Locate every malaria parasite by life-cycle stage, and every leukocyte.
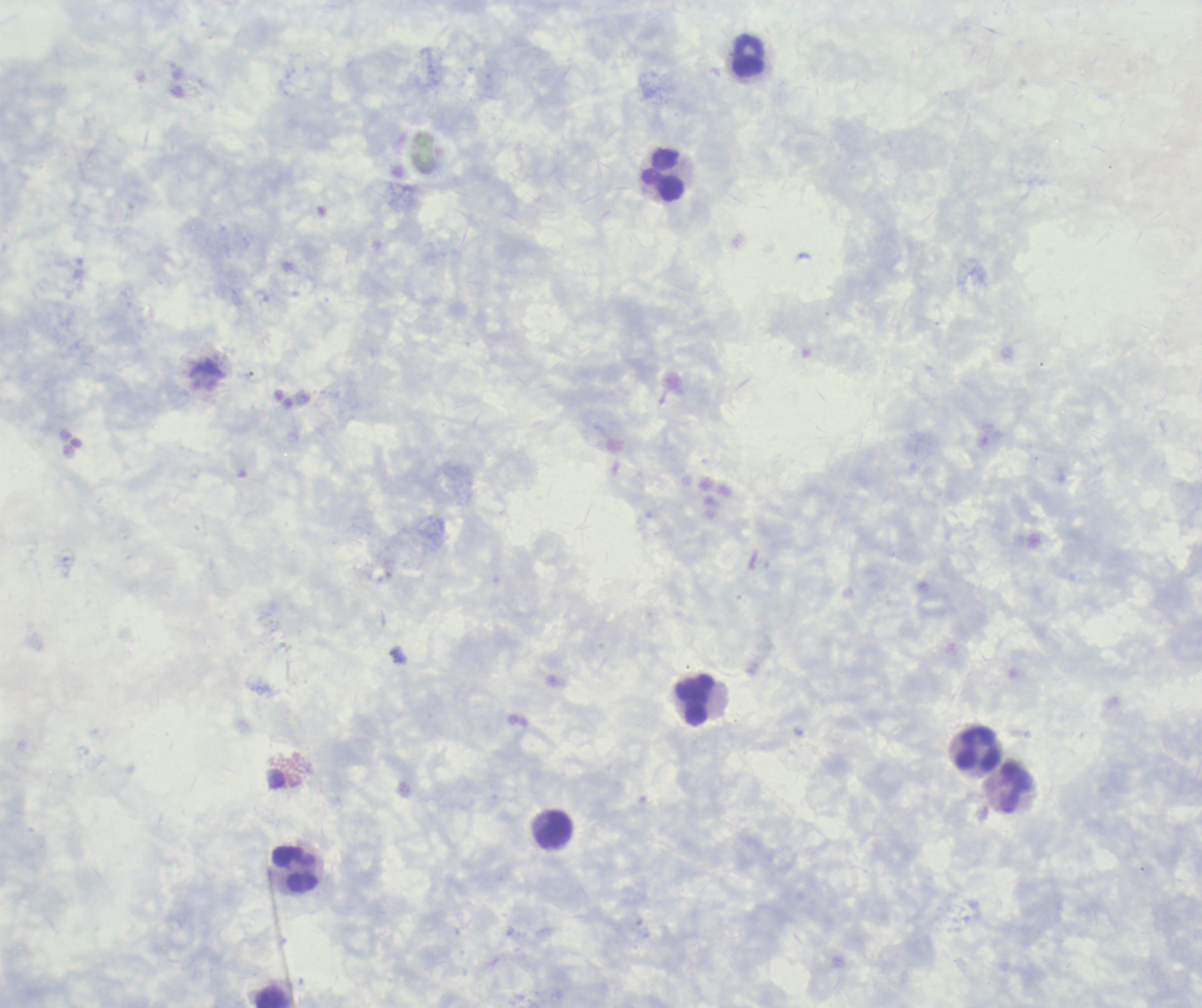

No malaria parasites seen.
Approximate object centers, in pixels from the top-left corner.
Leukocytes: (x=748, y=55), (x=662, y=175), (x=695, y=700), (x=979, y=749), (x=1017, y=787), (x=554, y=829), (x=296, y=870), (x=274, y=997).

Captured at 100x magnification. Coloration quality: good. Thick smear of blood. Previously used in an actual diagnosis. Background quality: unsatisfactory. Image is 1202×1008 pixels. Single field of view. Romanowsky-stained preparation.